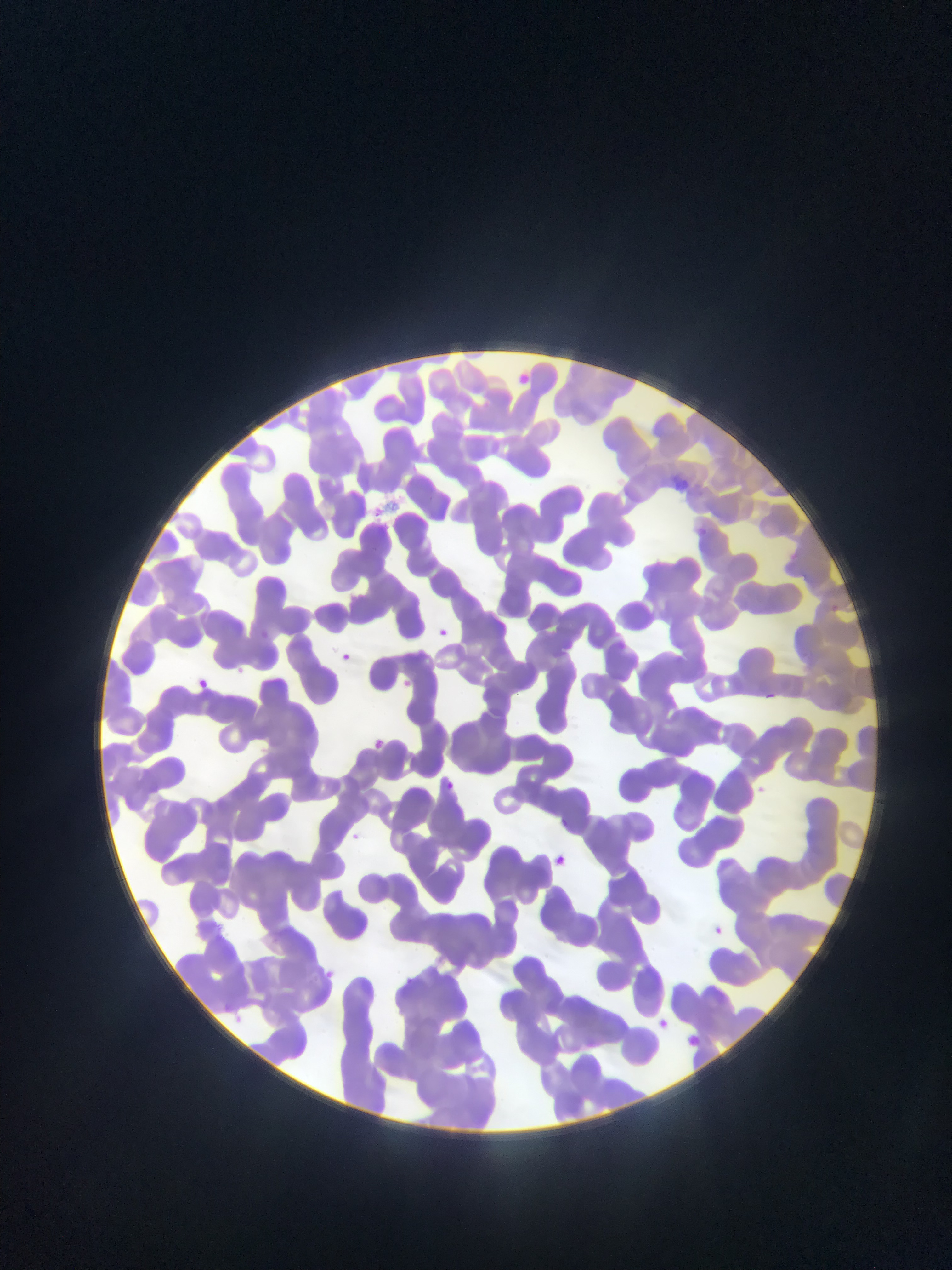

{
  "image_size": "952×1270 pixels",
  "malaria_parasite_locations": "approximate bounding boxes as {left, top, right, bottom} in pixels: {518, 370, 535, 388}, {670, 472, 701, 496}, {253, 623, 274, 639}, {435, 624, 452, 635}, {617, 630, 639, 656}, {341, 647, 363, 673}, {229, 661, 254, 678}, {399, 675, 417, 689}, {198, 676, 211, 688}, {760, 687, 781, 704}, {370, 737, 395, 754}, {440, 773, 463, 789}, {749, 783, 773, 798}, {348, 823, 376, 848}, {547, 848, 564, 865}, {709, 918, 729, 937}, {324, 960, 338, 979}, {405, 976, 424, 989}, {651, 1010, 672, 1031}, {683, 1029, 699, 1048}",
  "preparation": "thin blood smear",
  "country": "Ghana",
  "field_of_view": "single",
  "capture": "mobile-phone photograph through a microscope"
}